Give the preparation type.
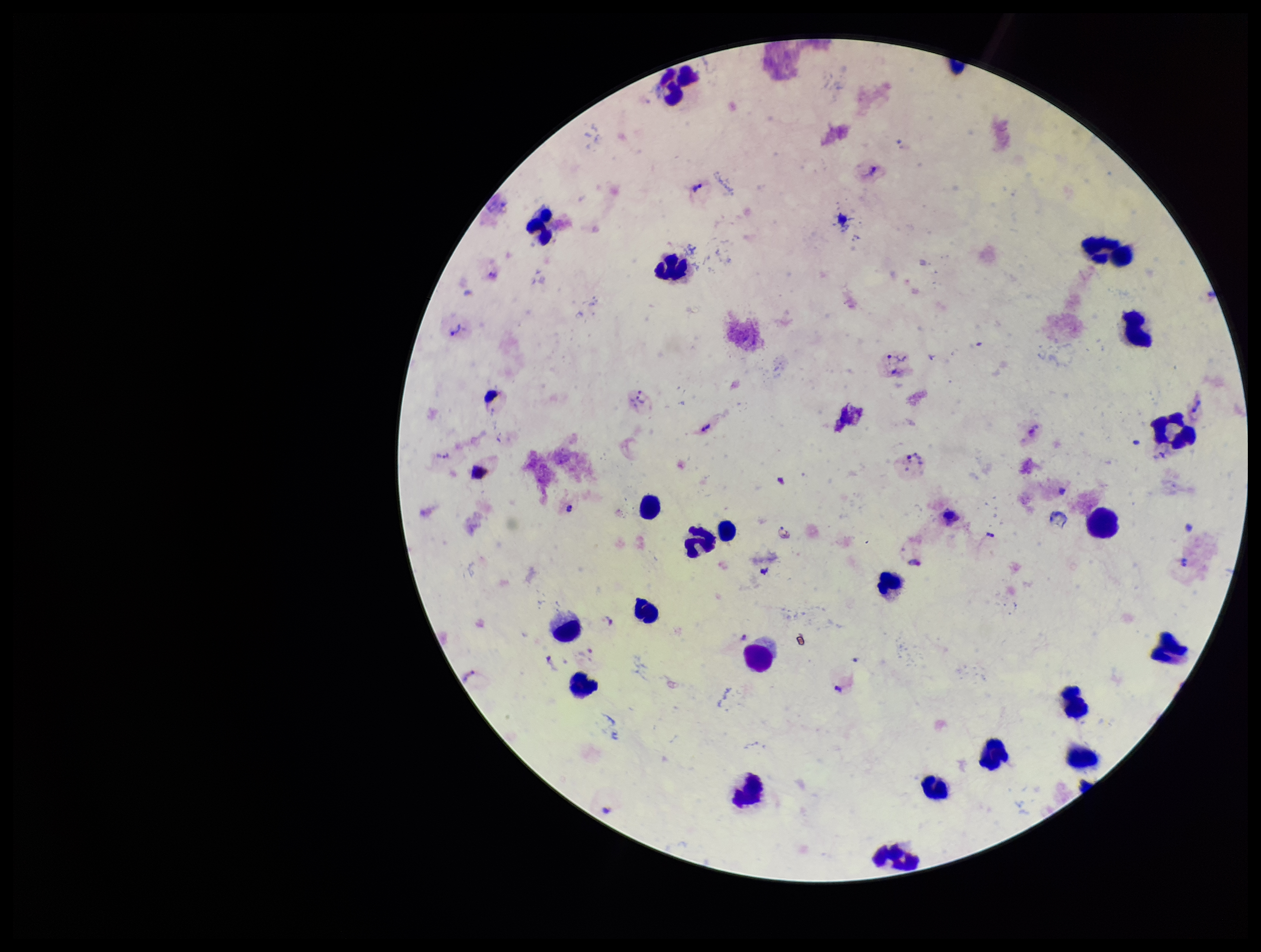

A thick smear.

Summary:
  - Field of view: single
  - Plasmodium parasites: seen
  - Capture: smartphone photograph through the microscope eyepiece
  - Species reported for this patient: Plasmodium vivax
  - Patient malaria status: positive
  - Stain: Giemsa
  - Leukocyte count: 22
  - Parasite count: 5
  - Image size: 1261×952 pixels